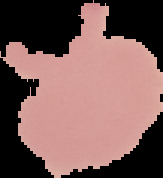

Summary:
  - Result: no malaria parasites seen
  - Image type: segmented cell region on a black background
  - Preparation: thin blood film
  - Image size: 163×178 pixels